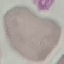 Result: no malaria parasites detected. Giemsa-stained preparation. Thin blood smear. Cell patch, automatically extracted from a larger field of view and resized to 64 × 64 pixels. Acquired by smartphone through the microscope eyepiece.